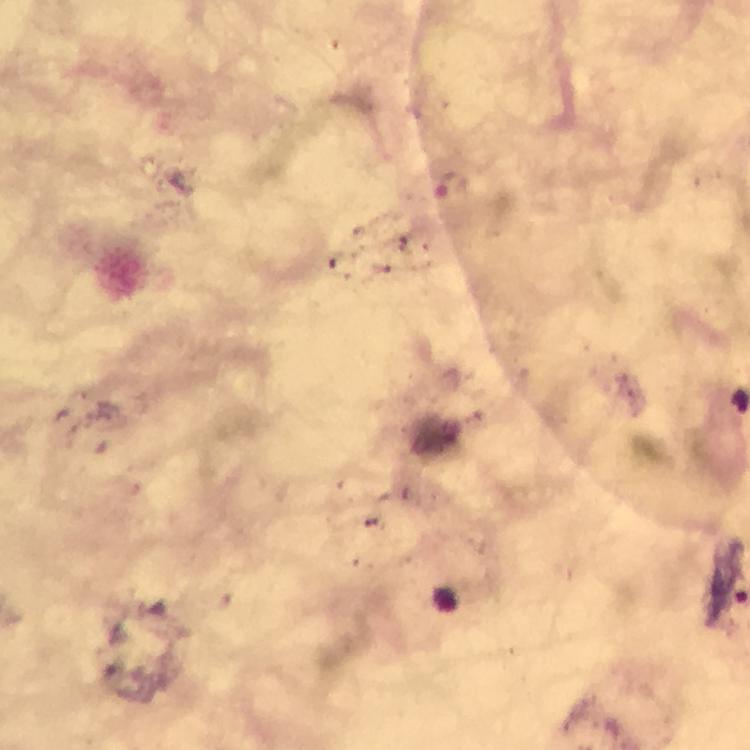

Approximate object centers, in pixels from the top-left corner.
Summary:
  - Plasmodium parasite locations: (x=450, y=186)
  - Preparation: thick smear
  - Image size: 750×750 pixels
  - Immersion oil: applied
  - Capture: smartphone photograph through a microscope
  - Cropped from: one field of view
  - Stain: Giemsa
  - Magnification: 100x
  - Context: from a malaria diagnostic workup